Classify this cell by malaria status.
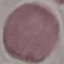
It is uninfected.

Summary:
  - Stain: Giemsa
  - Image type: automatically extracted cell patch, resized to 64 × 64 pixels
  - Preparation: thin smear
  - Capture: smartphone camera at the microscope eyepiece